Locate every P. falciparum parasite and give its life-cycle stage, and locate every leukocyte and any debris.
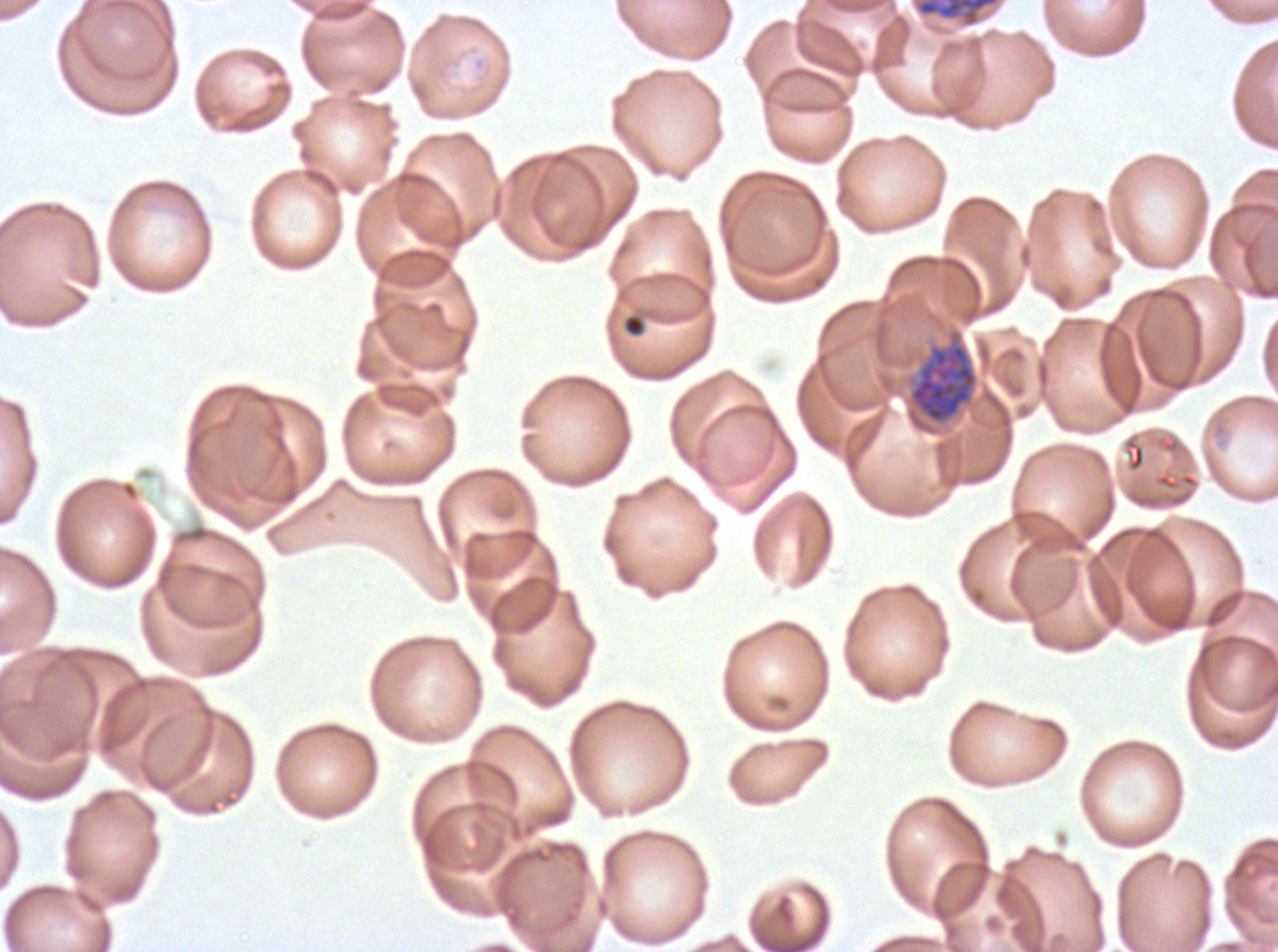

Approximate bounding boxes as {x1, y1, x2, y2} in pixels.
Early schizonts: {914, 0, 1001, 29}, {908, 329, 978, 425}.
Debris: {622, 313, 646, 337}, {173, 524, 223, 544}.
No rings, late-ring/early-trophozoite forms, mid trophozoites, late trophozoites, late schizonts, segmenters, gametocytes, or leukocytes observed.

One sub-image of a larger composite. P. falciparum cultured ex vivo for 24 to 48 hours, from a patient in The Gambia. Thin blood smear. Image is 1278×952 pixels. Giemsa-stained preparation.